Assess for malaria.
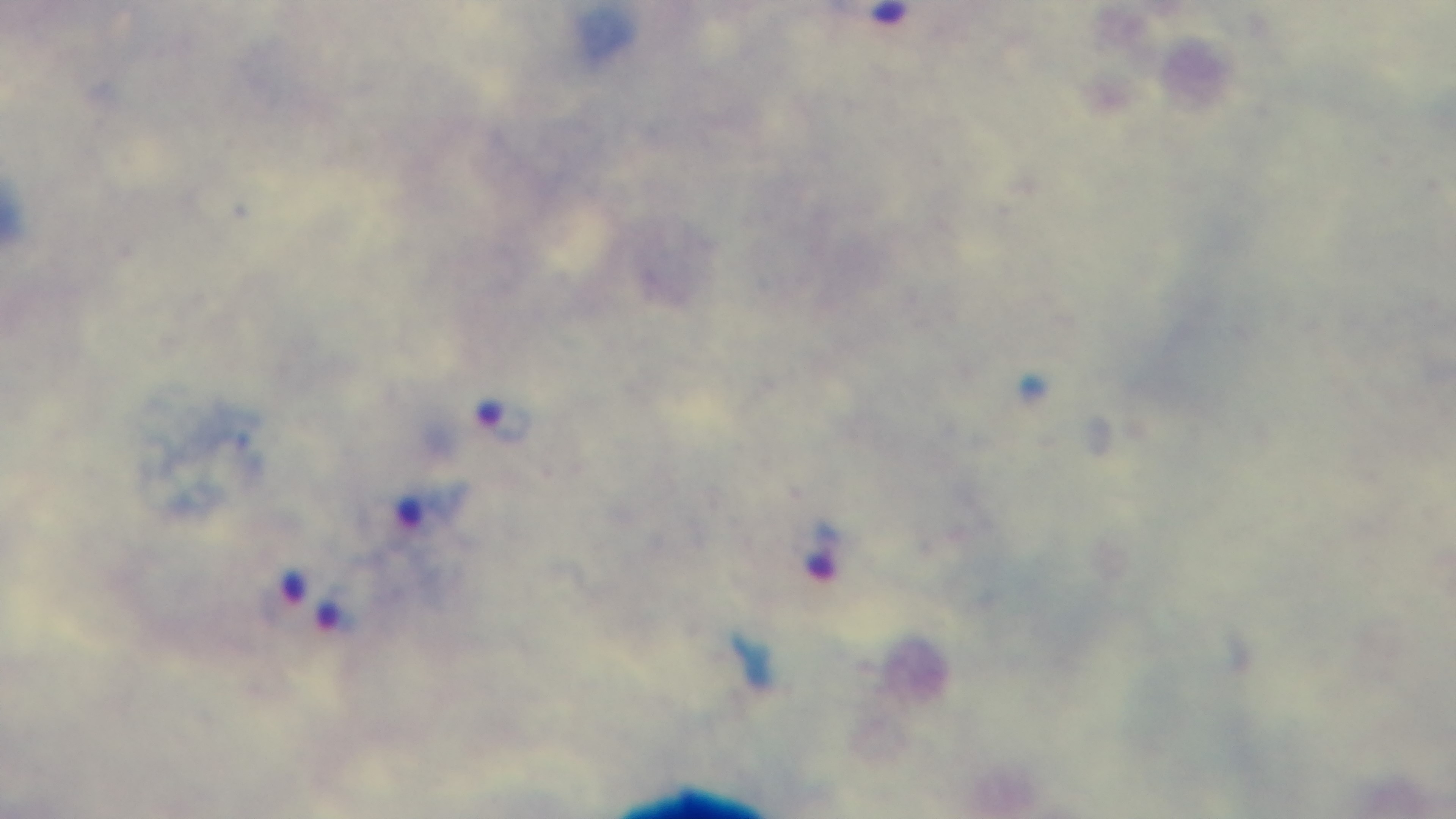
Positive.

Single field of view. Preparation: thick smear. Captured with a mounted 4K digital camera. Giemsa stain. Photomicrograph. 100x oil-immersion objective.